Assess this cell for malaria.
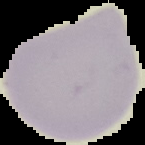

Uninfected.

image size = 145×145 pixels
image type = cell region segmented out of the field of view; surrounding area masked to black
preparation = thin blood film